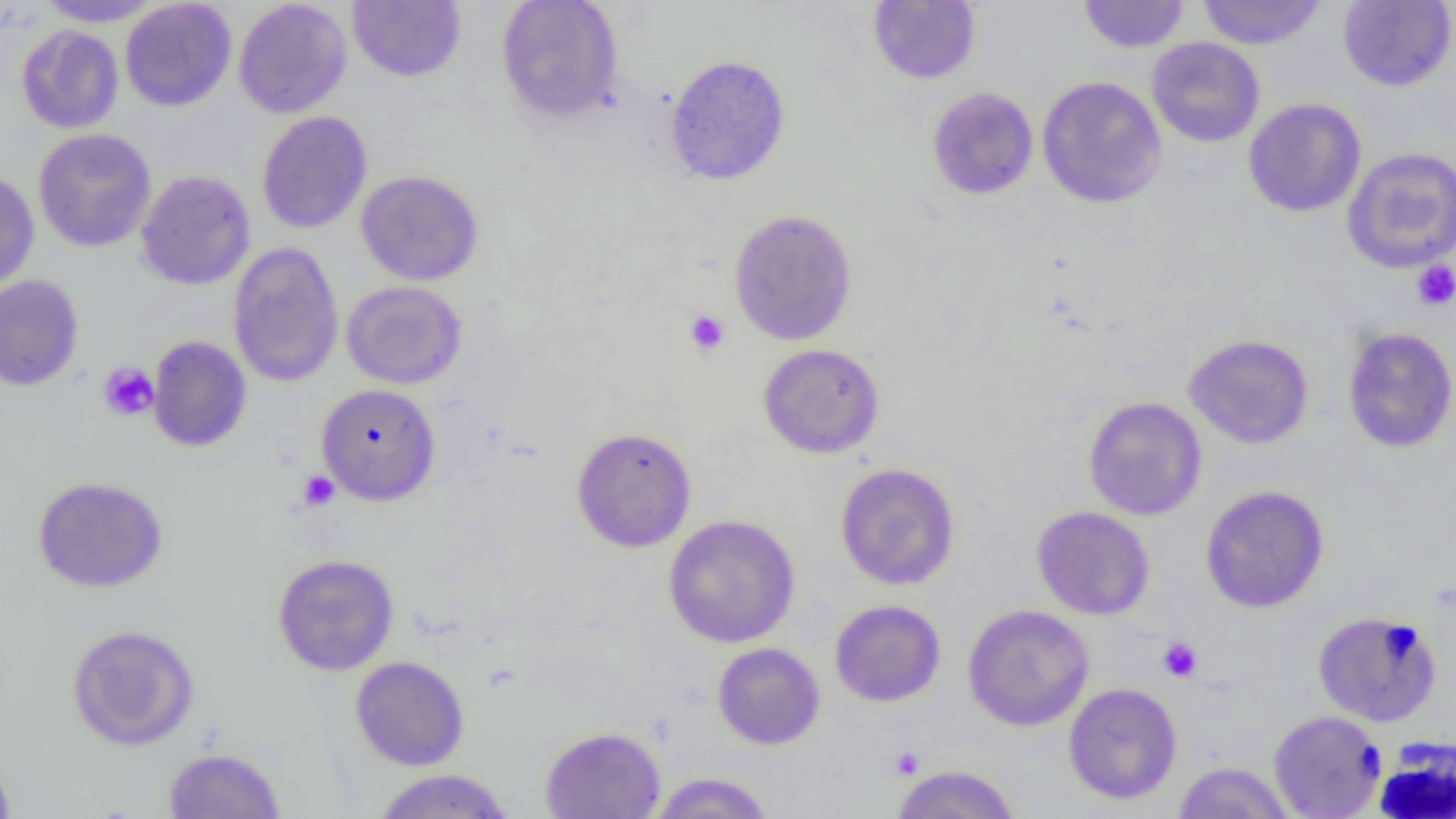
slide-level diagnosis = negative for blood parasites
platelet locations = approximate bounding boxes as (x1,y1)-(x2,y2) corner pairs in pixels: (1411,261)-(1456,312), (684,310)-(729,356), (98,362)-(159,422), (297,470)-(340,511), (1157,636)-(1203,683), (889,747)-(924,779)
field of view = one of a larger specimen
magnification = 1000x
image size = 1456×819 pixels
modality = light microscopy
preparation = thin blood smear
uninfected red blood cell locations = approximate bounding boxes as (x1,y1)-(x2,y2) corner pairs in pixels: (34,0)-(163,27), (234,0)-(352,118), (347,0)-(466,82), (496,0)-(624,122), (1077,0)-(1190,54), (1197,0)-(1327,50), (120,1)-(237,111), (868,1)-(981,84), (1337,1)-(1456,91), (17,19)-(238,123), (16,24)-(124,134), (1146,37)-(1265,147), (665,54)-(790,185), (1037,76)-(1167,208), (926,87)-(1039,200), (1243,98)-(1366,217), (256,111)-(372,234), (32,128)-(157,252), (1342,146)-(1456,273), (0,169)-(39,291), (136,170)-(255,290), (356,170)-(484,286), (728,208)-(857,346), (228,242)-(344,387), (0,274)-(84,392), (341,281)-(467,389), (1341,326)-(1456,454), (1183,333)-(1314,449), (147,336)-(252,453), (758,343)-(885,459), (316,383)-(441,506), (1083,396)-(1207,521), (570,426)-(697,552), (834,463)-(960,591), (32,475)-(168,593), (1200,485)-(1329,613), (1031,506)-(1155,620), (663,514)-(801,648), (272,553)-(399,676), (830,599)-(946,707), (962,604)-(1094,731), (1312,611)-(1442,727), (66,623)-(199,750), (712,642)-(825,750), (350,655)-(470,771), (1063,682)-(1182,805), (1268,710)-(1386,818), (539,726)-(666,819), (163,746)-(286,818), (0,750)-(16,818), (1172,761)-(1295,819), (890,764)-(1021,819), (371,768)-(514,818), (648,772)-(775,818)